Assess the morphology of the red blood cells.
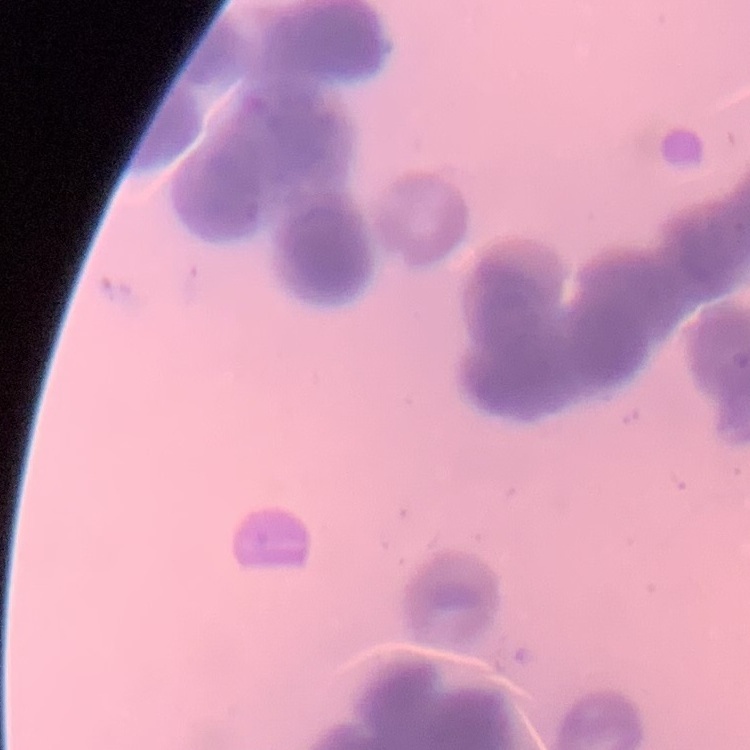
They show rouleaux formation.

Stained with either Field's or Giemsa. Square crop of a larger photomicrograph. Thin blood smear.